Assess the morphology of the erythrocytes.
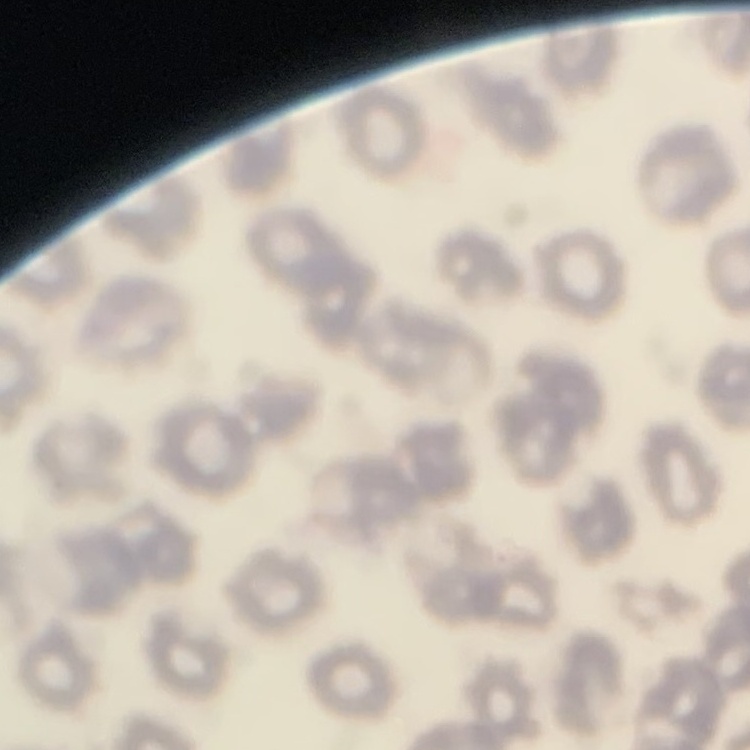
No rouleaux formation.

Summary:
  - Stain: Field's or Giemsa
  - Image type: one tile cut from a larger photomicrograph
  - Preparation: thin blood smear